Report the malaria status of this cell.
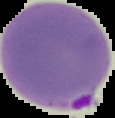

Parasitized.

Summary:
  - Image type: segmented cell region with the area outside set to black
  - Image size: 115×118 pixels
  - Preparation: thin blood smear